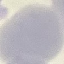

Summary:
  - Malaria status: uninfected
  - Stain: Giemsa
  - Image type: cell patch, automatically extracted from a larger field of view and resized to 64 × 64 pixels
  - Preparation: thin blood film
  - Capture: smartphone through the microscope eyepiece